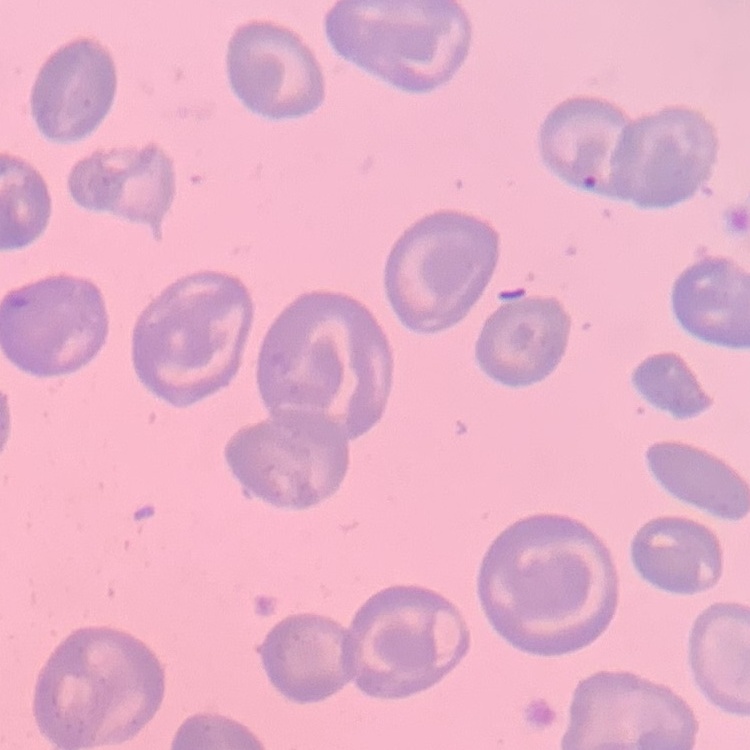

{
  "red_blood_cell_morphology": "no rouleaux formation",
  "preparation": "thin blood film",
  "stain": "Field's or Giemsa",
  "image_type": "square crop of a larger photomicrograph"
}